Describe the morphology of the erythrocytes.
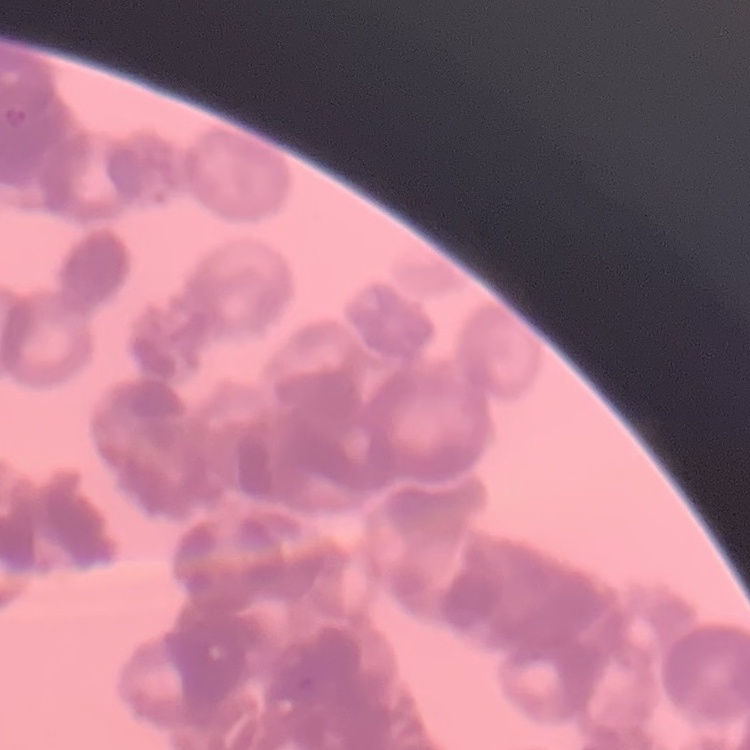
Rouleaux formation.

stain = Field's or Giemsa
preparation = thin blood smear
image type = one tile cut from a larger photomicrograph